Locate the P. falciparum-infected red blood cells and any of indeterminate infection status.
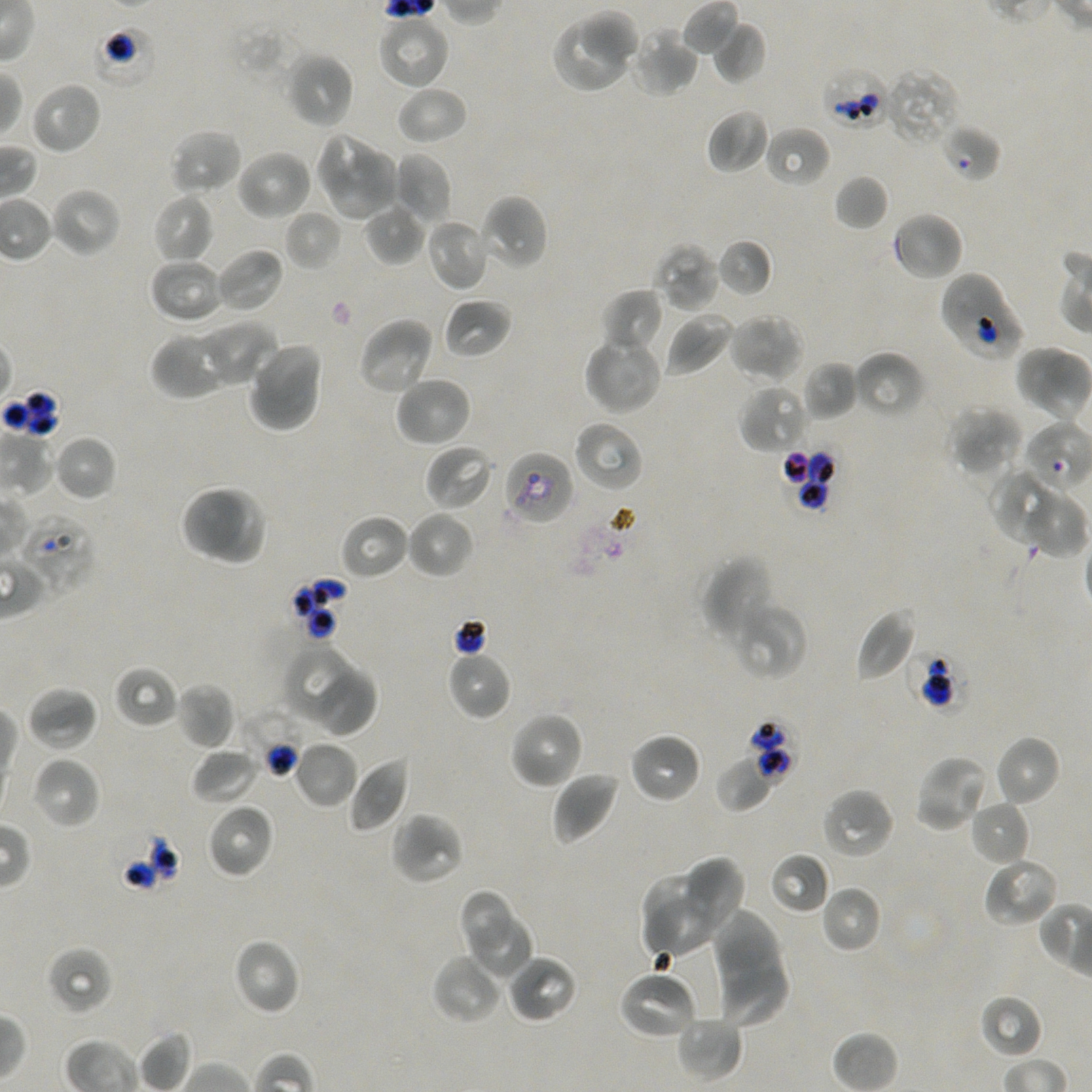

Approximate bounding boxes as (x1, y1, x2, y2) in pixels. Not every red blood cell is marked.
Red blood cells of indeterminate infection status: (91, 23, 158, 90), (820, 67, 891, 130), (940, 124, 1002, 182), (939, 270, 1027, 363), (1023, 422, 1092, 492), (782, 447, 837, 511), (502, 449, 574, 525), (17, 513, 96, 596), (908, 647, 969, 712), (241, 708, 310, 779), (108, 825, 181, 894).
No infected red blood cells observed.

Summary:
  - Locations of uninfected red blood cells: (579, 10, 642, 67), (376, 13, 450, 90), (550, 18, 630, 94), (712, 20, 767, 84), (627, 28, 699, 97), (285, 51, 355, 129), (884, 66, 961, 147), (29, 81, 103, 156), (395, 86, 468, 145), (706, 108, 770, 175), (764, 126, 831, 188), (168, 128, 242, 196), (314, 132, 382, 202), (236, 149, 314, 221), (330, 151, 396, 221), (394, 153, 453, 223), (833, 174, 889, 231), (49, 187, 122, 258), (153, 194, 215, 265), (479, 194, 549, 272), (363, 202, 424, 266), (284, 208, 344, 270), (892, 211, 964, 282), (424, 217, 492, 292), (716, 238, 773, 297), (653, 242, 722, 312), (215, 247, 285, 314), (149, 257, 226, 324), (600, 289, 663, 356), (443, 297, 511, 359), (663, 312, 735, 376), (729, 312, 805, 384), (358, 316, 435, 397), (201, 321, 277, 386), (151, 331, 232, 399), (583, 333, 663, 416), (247, 340, 324, 433), (1015, 344, 1073, 412), (852, 350, 925, 418), (801, 360, 858, 421), (393, 375, 471, 448), (739, 384, 809, 454), (946, 405, 1023, 477), (572, 419, 644, 493), (53, 435, 117, 502), (424, 445, 494, 511), (989, 467, 1059, 543), (181, 484, 250, 561), (196, 484, 270, 568), (1025, 490, 1087, 558), (405, 510, 475, 579), (339, 513, 410, 581), (701, 556, 775, 644), (734, 608, 807, 680), (855, 608, 917, 682), (283, 645, 359, 723), (445, 649, 511, 721), (113, 665, 179, 728), (316, 668, 380, 742), (175, 682, 236, 750), (26, 685, 98, 751), (508, 710, 585, 790), (629, 731, 703, 805), (994, 734, 1061, 807), (294, 740, 358, 809), (190, 746, 261, 805), (914, 754, 991, 834), (714, 755, 775, 814), (31, 756, 101, 830), (348, 757, 411, 833), (551, 769, 621, 845), (820, 786, 896, 860), (969, 799, 1030, 865), (206, 803, 275, 879), (389, 811, 466, 886), (769, 852, 831, 915), (680, 856, 746, 937), (982, 856, 1060, 929), (640, 873, 719, 936), (820, 884, 882, 953), (458, 889, 514, 960), (641, 894, 729, 959), (465, 909, 535, 983), (710, 911, 781, 994), (232, 938, 301, 1016), (46, 946, 113, 1015), (431, 953, 505, 1025), (507, 954, 578, 1023), (715, 966, 789, 1030), (617, 970, 698, 1041), (979, 994, 1044, 1060), (676, 1015, 744, 1080), (138, 1030, 192, 1092)
  - Stain: Giemsa
  - Field of view: one from this slide
  - Culture: static in-vitro P. falciparum strain NF54
  - Preparation: thin blood smear
  - Objective: 100x, oil immersion, numerical aperture 1.45
  - Image size: 1092×1092 pixels
  - Donor blood group: A+/O+